Classify this cell by malaria status.
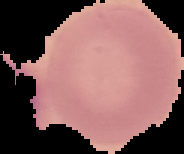
It is uninfected.

preparation = thin blood film
image type = cell region segmented out of the field of view; surrounding area masked to black
image size = 184×154 pixels